Classify this cell by malaria status.
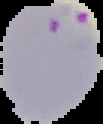

Parasitized.

image type = segmented cell region with the area outside set to black
preparation = thin blood film
image size = 103×124 pixels